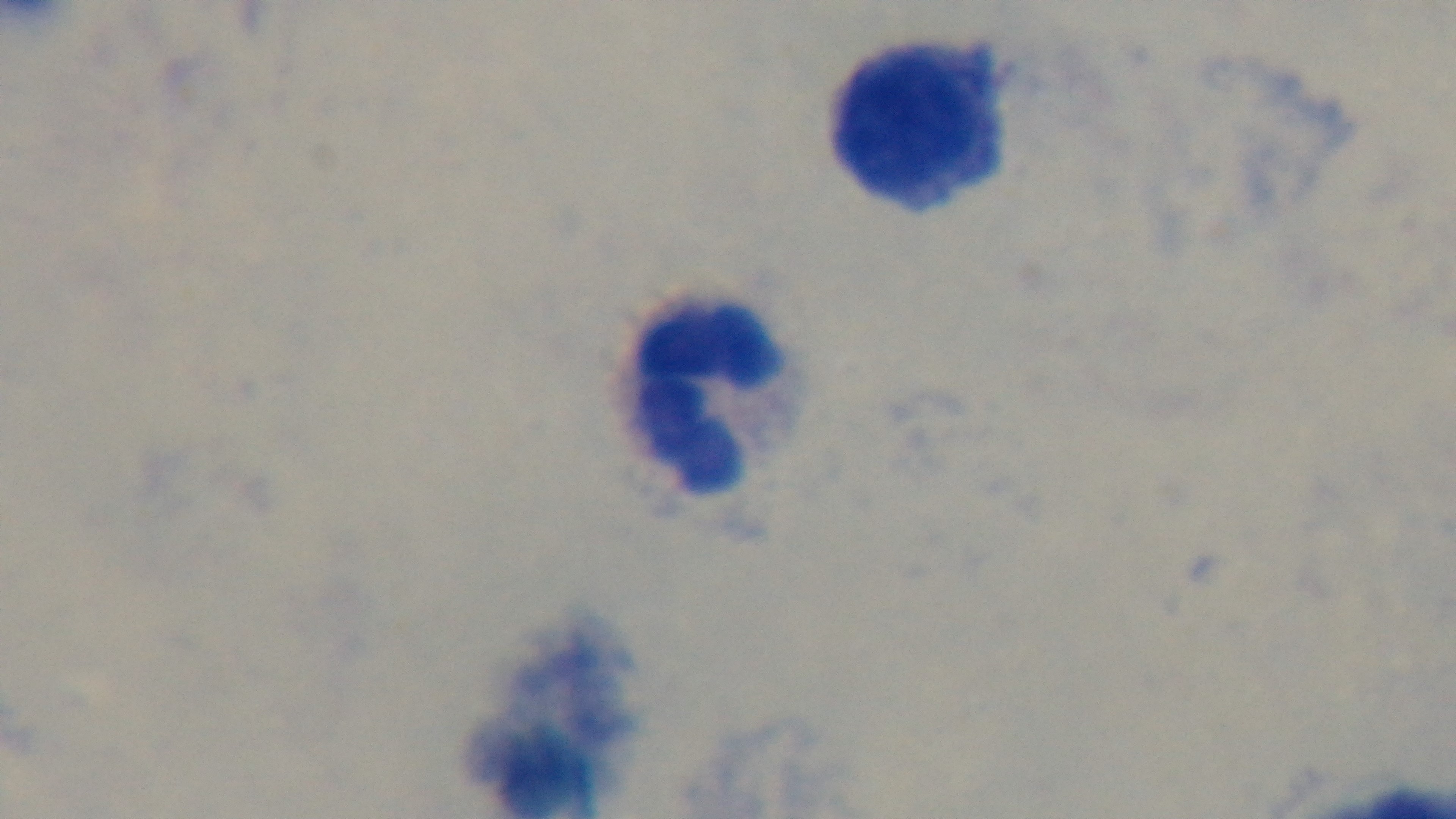

Malaria status: negative. One field from the slide. 100x oil-immersion objective. Captured with a mounted 4K digital camera. Giemsa-stained. Preparation: thick. Photomicrograph.